Evaluate for Plasmodium parasites.
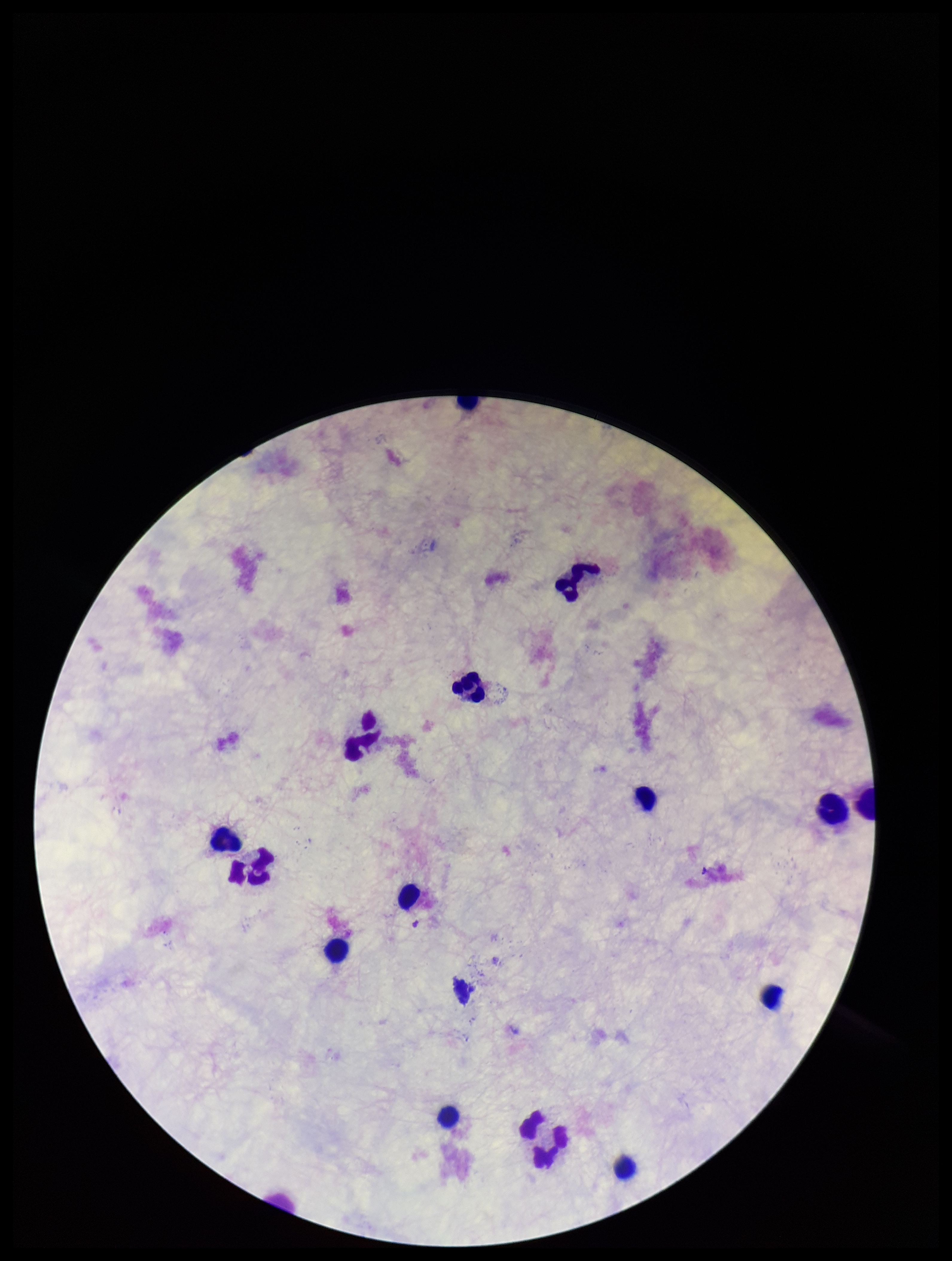
None detected.

Giemsa stain. One field from this slide. Parasite count: 0. Patient malaria status: negative. Photographed through the microscope eyepiece with a smartphone camera. Image is 952×1261 pixels. Leukocyte count: 15. Preparation: thick blood smear.